Mark where platelets are.
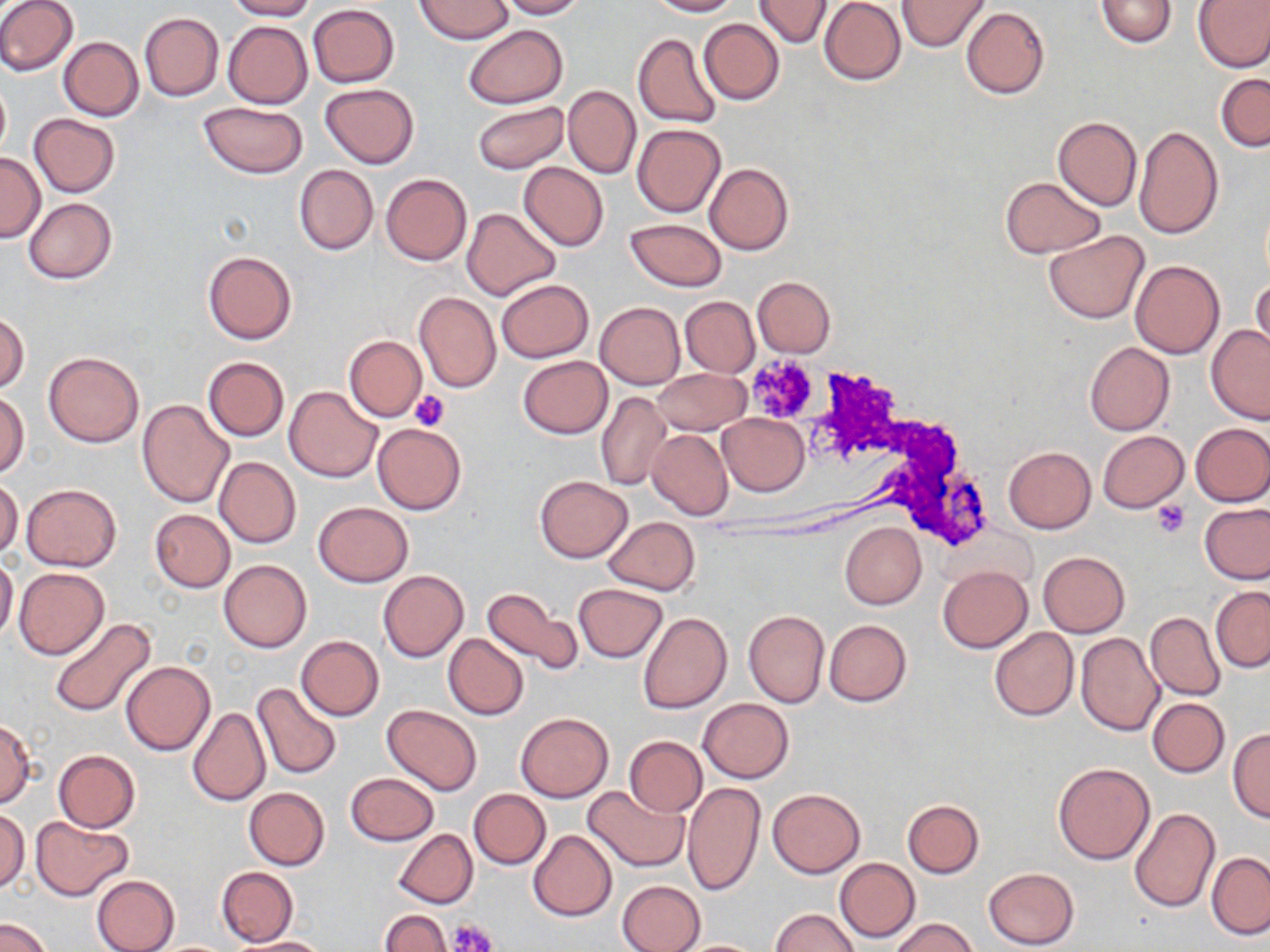

Approximate bounding boxes as (x1,y1)-(x2,y2) corner pairs in pixels.
Platelets: (744,356)-(820,424), (411,390)-(450,431), (1151,500)-(1191,537), (450,918)-(497,952).

slide-level diagnosis = no evidence of blood parasites
image size = 1270×952 pixels
uninfected red blood cell locations = approximate bounding boxes as (x1,y1)-(x2,y2) corner pairs in pixels: (0,0)-(78,76), (226,0)-(316,20), (497,0)-(587,19), (647,0)-(739,16), (819,0)-(906,85), (897,0)-(989,51), (1095,0)-(1177,48), (1193,0)-(1270,72), (415,1)-(512,43), (754,1)-(832,47), (308,4)-(399,87), (313,6)-(404,169), (960,6)-(1050,98), (138,12)-(224,101), (699,19)-(784,104), (223,21)-(311,107), (463,24)-(569,109), (632,32)-(723,130), (58,36)-(144,120), (1215,73)-(1270,152), (0,77)-(10,163), (320,84)-(419,168), (563,84)-(640,179), (472,99)-(568,174), (199,102)-(307,178), (27,113)-(120,197), (1053,115)-(1141,210), (632,123)-(725,217), (1134,125)-(1224,242), (0,152)-(44,242), (518,162)-(608,251), (704,163)-(793,255), (294,164)-(377,255), (380,174)-(472,265), (1000,176)-(1104,258), (24,198)-(116,283), (461,207)-(560,301), (625,218)-(727,291), (1044,231)-(1149,324), (202,250)-(297,345), (1131,261)-(1225,359), (1251,274)-(1269,359), (752,275)-(835,356), (495,279)-(593,363), (413,291)-(500,393), (680,296)-(759,377), (595,302)-(685,389), (0,312)-(28,393), (1205,325)-(1270,424), (344,335)-(427,421), (1084,341)-(1175,435), (44,352)-(143,447), (519,355)-(612,438), (202,356)-(290,441), (654,368)-(749,435), (284,386)-(383,482), (597,390)-(669,492), (1,391)-(29,478), (137,400)-(234,507), (718,413)-(809,497), (1190,422)-(1270,506), (372,423)-(466,514), (646,429)-(733,520), (1097,431)-(1189,513), (1004,445)-(1096,532), (215,456)-(301,549), (534,475)-(633,563), (0,478)-(23,559), (21,483)-(121,571), (313,501)-(413,586), (1200,502)-(1270,585), (149,509)-(236,592), (604,516)-(700,595), (840,522)-(926,610), (1037,552)-(1129,637), (0,557)-(18,644), (220,559)-(311,652), (938,565)-(1032,652), (14,567)-(109,660), (378,570)-(468,662), (573,583)-(669,662), (1211,586)-(1270,672), (481,587)-(582,676), (743,610)-(830,708), (1146,611)-(1226,700), (639,612)-(732,714), (49,617)-(156,718), (824,620)-(911,706), (989,627)-(1080,721), (443,633)-(528,719), (1075,633)-(1163,737), (296,636)-(384,720), (121,660)-(214,755), (251,681)-(342,779), (698,698)-(794,783), (1148,698)-(1228,777), (382,704)-(483,796), (188,706)-(270,806), (516,712)-(613,802), (0,719)-(37,808), (1228,728)-(1270,822), (625,736)-(708,817), (53,749)-(141,832), (1053,762)-(1155,864), (346,771)-(438,846), (682,781)-(765,897), (583,783)-(689,873), (244,787)-(329,870), (469,788)-(550,869), (767,788)-(865,878), (901,799)-(984,878), (0,806)-(29,893), (1128,807)-(1220,912), (30,815)-(134,900), (394,829)-(478,909), (528,830)-(617,921), (1207,852)-(1270,939), (834,858)-(920,942), (216,867)-(297,945), (983,867)-(1079,950), (91,874)-(179,952), (617,879)-(706,952), (772,909)-(859,952), (378,910)-(450,952), (0,915)-(54,952), (891,917)-(977,952), (230,936)-(331,951), (672,939)-(771,951)
magnification = 1000x
stain = May-Grünwald-Giemsa
field of view = one of a larger specimen
modality = light microscopy
preparation = thin blood smear